Give the position of every Plasmodium parasite.
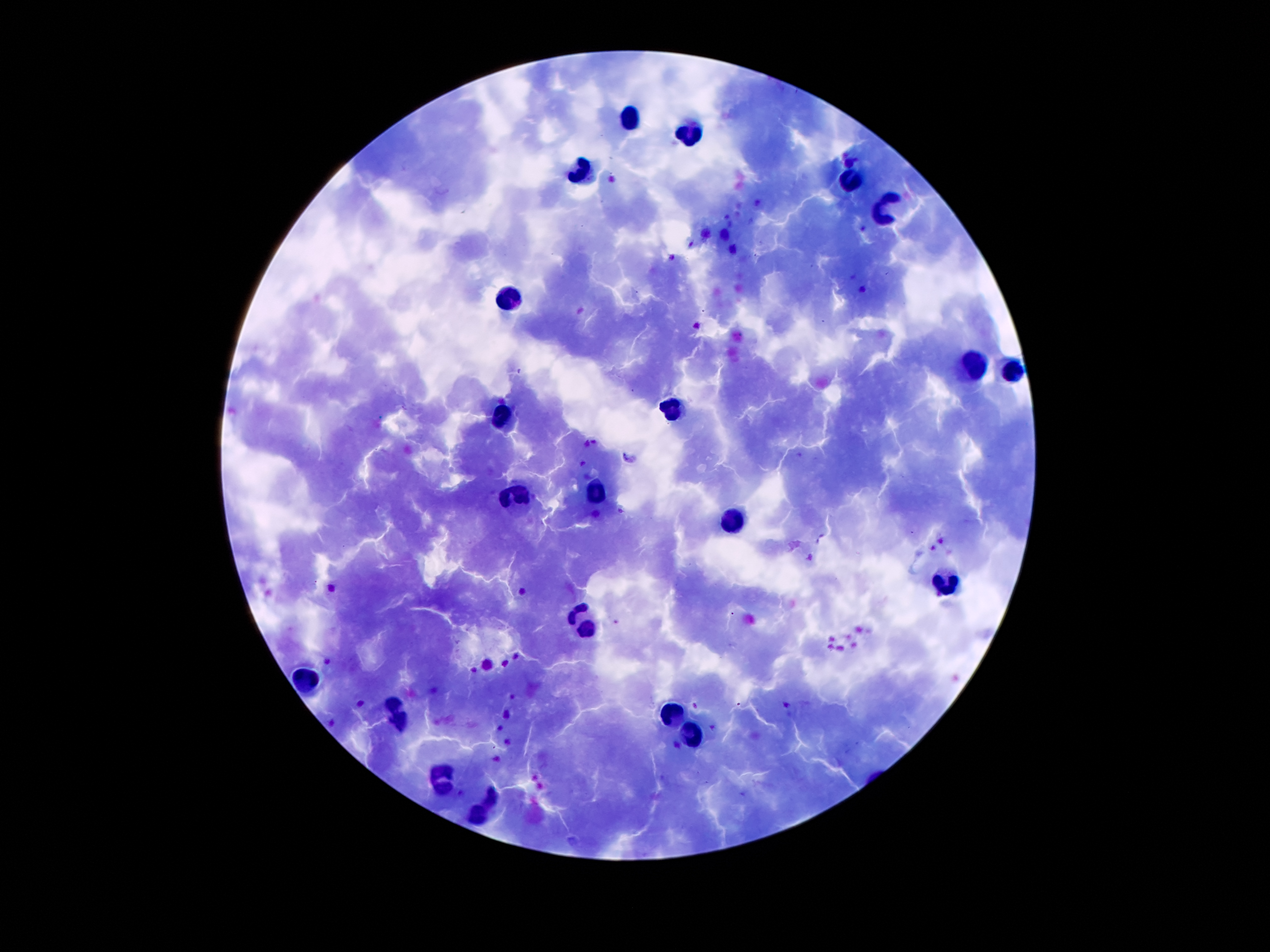
Approximate object centers, in pixels from the top-left corner.
Plasmodium parasites: (x=672, y=258), (x=630, y=459).

Summary:
  - Leukocyte locations: (x=635, y=121), (x=693, y=131), (x=581, y=169), (x=853, y=181), (x=885, y=205), (x=509, y=301), (x=975, y=363), (x=1013, y=369), (x=675, y=411), (x=499, y=415), (x=519, y=491), (x=595, y=491), (x=733, y=519), (x=945, y=581), (x=585, y=626), (x=306, y=678), (x=396, y=704), (x=674, y=714), (x=401, y=724), (x=692, y=736), (x=445, y=769), (x=443, y=789), (x=492, y=798), (x=477, y=816)
  - Preparation: thick blood film
  - Patient malaria status: infected with Plasmodium falciparum
  - Stain: Giemsa
  - Field of view: one from this slide
  - Image size: 1270×952 pixels
  - Capture: smartphone through the microscope eyepiece
  - Magnification: 100x